Classify this cell by malaria status.
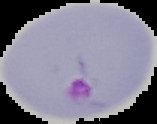

It is parasitized.

preparation = thin blood smear
image type = cell region segmented out of the field of view; surrounding area masked to black
image size = 157×124 pixels